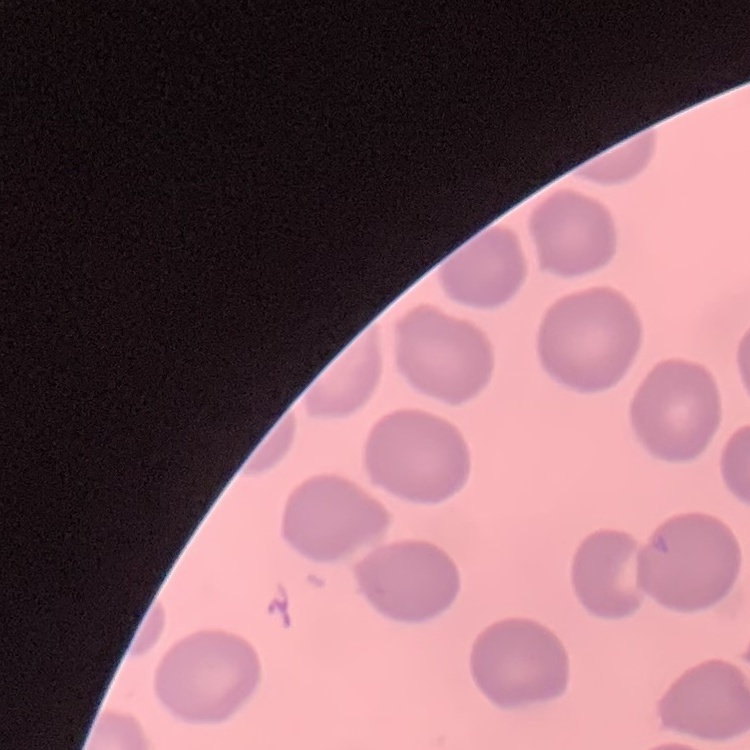

{
  "red_blood_cell_morphology": "no rouleaux formation",
  "image_type": "one tile cut from a larger photomicrograph",
  "stain": "Field's or Giemsa",
  "preparation": "thin blood film"
}